State which cell type is depicted.
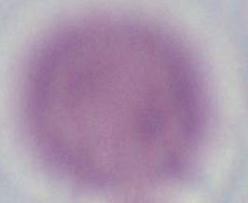
An erythrocyte.

modality = micrograph
magnification = 1000x